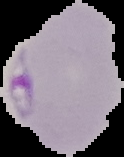
Image is 124×157 pixels. Result: Plasmodium parasites identified. The area outside the segmented cell region is set to black. From a thin blood film.